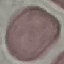
Summary:
  - Result: negative for malaria parasites
  - Capture: smartphone through the microscope eyepiece
  - Preparation: thin blood smear
  - Image type: cell patch, automatically extracted from a larger field of view and resized to 64 × 64 pixels
  - Stain: Giemsa